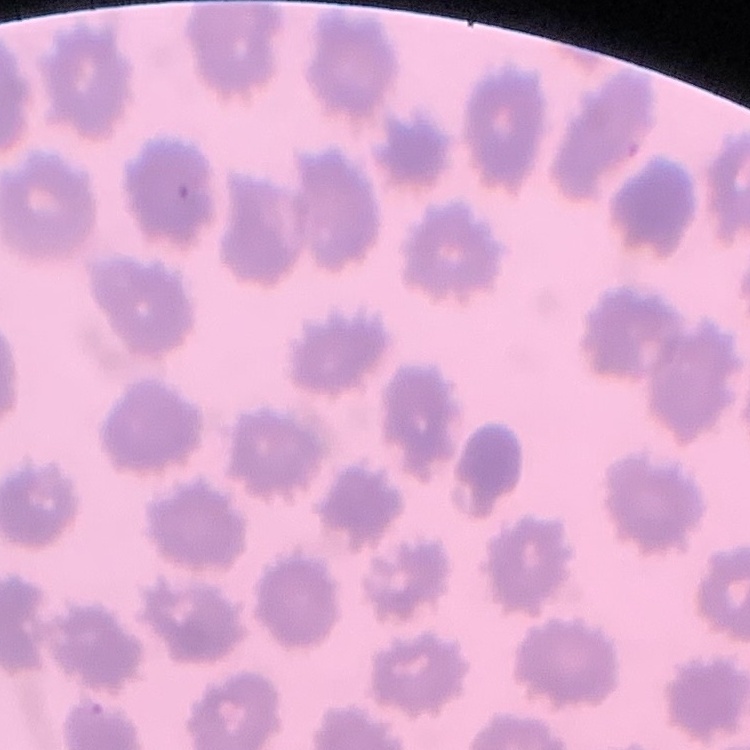

Summary:
  - Erythrocyte morphology: no rouleaux formation
  - Preparation: thin blood smear
  - Image type: one tile cut from a larger photomicrograph
  - Stain: Field's or Giemsa